Name the blood parasite species.
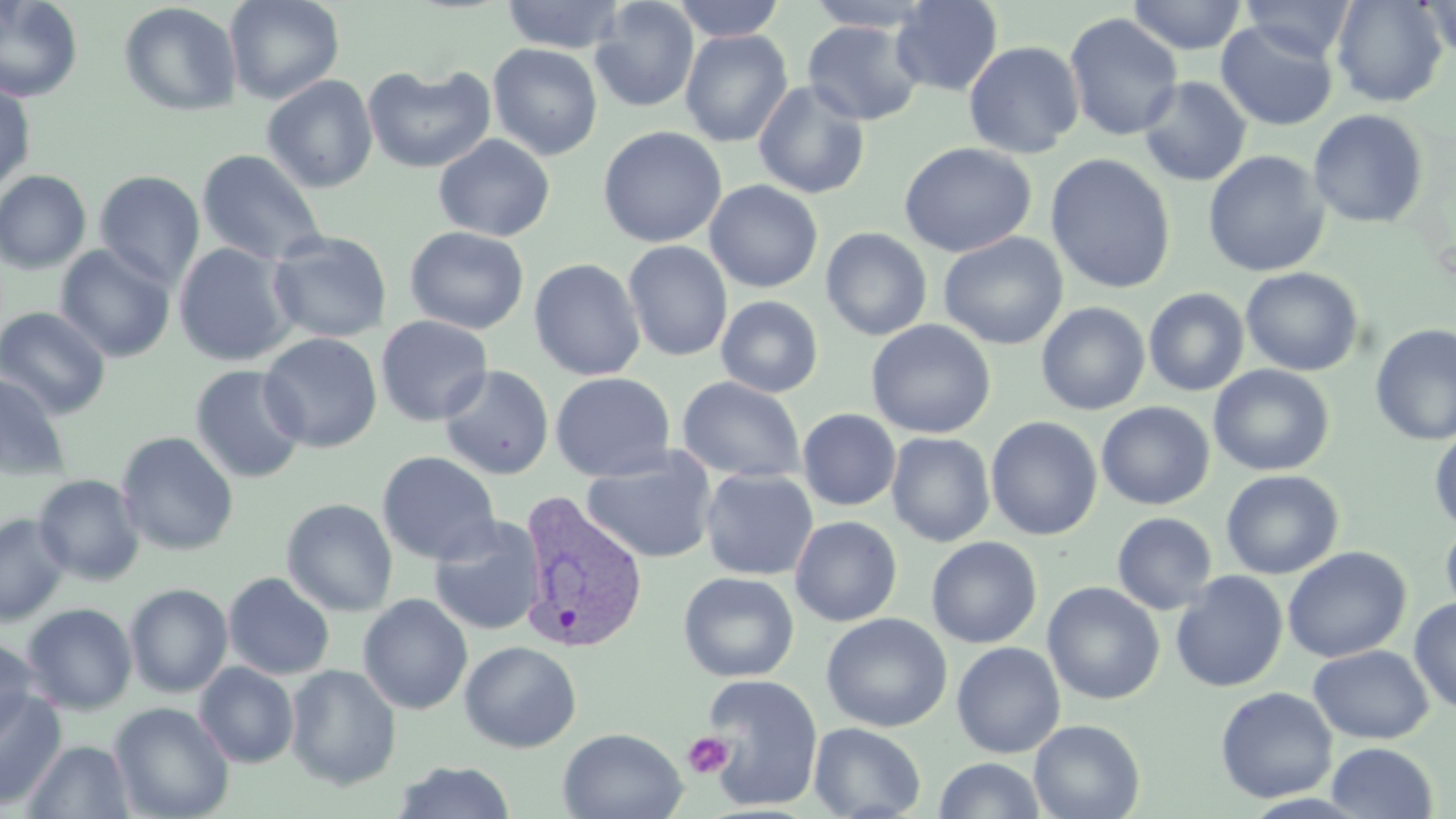
Plasmodium vivax.

{
  "preparation": "thin blood film",
  "plasmodium_vivax_infected_red_blood_cell_locations": "approximate bounding boxes as [x1, y1, x2, y2] in pixels: [517, 491, 650, 655]",
  "magnification": "1000x",
  "field_of_view": "single",
  "uninfected_red_blood_cell_locations": "approximate bounding boxes as [x1, y1, x2, y2] in pixels: [0, 0, 84, 102], [225, 0, 344, 104], [501, 0, 626, 54], [589, 0, 700, 113], [671, 0, 785, 42], [803, 0, 939, 32], [890, 0, 1004, 96], [1127, 0, 1247, 55], [1240, 0, 1357, 62], [1330, 0, 1448, 108], [1416, 0, 1455, 61], [118, 2, 243, 118], [1063, 13, 1184, 141], [801, 20, 924, 126], [1216, 20, 1339, 131], [679, 28, 793, 147], [963, 40, 1084, 159], [488, 43, 603, 160], [361, 64, 496, 174], [262, 75, 378, 193], [1138, 76, 1252, 187], [752, 79, 871, 200], [0, 81, 36, 192], [1308, 109, 1429, 229], [597, 126, 727, 248], [432, 134, 555, 242], [898, 142, 1037, 258], [196, 148, 327, 266], [1203, 150, 1329, 277], [1044, 153, 1176, 294], [0, 170, 92, 274], [93, 170, 205, 288], [704, 179, 823, 293], [405, 226, 530, 334], [820, 227, 933, 341], [266, 230, 392, 344], [938, 232, 1068, 350], [622, 240, 733, 362], [173, 242, 298, 366], [55, 244, 176, 363], [528, 258, 646, 381], [1241, 267, 1364, 376], [1143, 287, 1250, 397], [716, 295, 824, 398], [1036, 301, 1151, 415], [0, 306, 111, 419], [375, 315, 493, 427], [865, 319, 996, 439], [1370, 323, 1456, 447], [259, 332, 382, 453], [189, 364, 308, 484], [1209, 364, 1335, 477], [438, 365, 555, 480], [0, 372, 71, 481], [550, 372, 677, 483], [677, 376, 806, 483], [1095, 401, 1215, 510], [797, 408, 901, 511], [985, 416, 1103, 541], [1429, 425, 1456, 533], [115, 431, 239, 556], [886, 432, 996, 547], [580, 447, 718, 564], [376, 451, 501, 565], [699, 468, 818, 581], [1220, 469, 1344, 580], [33, 474, 145, 585], [281, 498, 399, 616], [1111, 512, 1217, 615], [0, 513, 71, 626], [427, 514, 547, 636], [790, 515, 903, 627], [1440, 517, 1456, 623], [926, 536, 1043, 649], [1282, 546, 1411, 663], [1170, 570, 1288, 692], [678, 571, 799, 682], [223, 572, 335, 680], [1042, 581, 1165, 705], [125, 583, 233, 698], [357, 593, 473, 715], [1409, 597, 1456, 714], [21, 603, 138, 715], [820, 612, 953, 733], [0, 637, 40, 744], [459, 641, 582, 753], [951, 641, 1066, 759], [1307, 645, 1435, 744], [194, 662, 299, 768], [285, 664, 402, 790], [698, 673, 824, 811], [1215, 686, 1338, 804], [0, 688, 66, 811], [109, 702, 235, 819], [1028, 719, 1144, 819], [809, 723, 925, 819], [559, 727, 687, 819], [21, 740, 135, 818], [1327, 742, 1438, 818], [934, 758, 1046, 817], [392, 761, 516, 819]",
  "image_size": "1456×819 pixels",
  "stain": "May-Grünwald-Giemsa",
  "platelet_locations": "approximate bounding boxes as [x1, y1, x2, y2] in pixels: [683, 732, 736, 779]",
  "modality": "light microscopy"
}